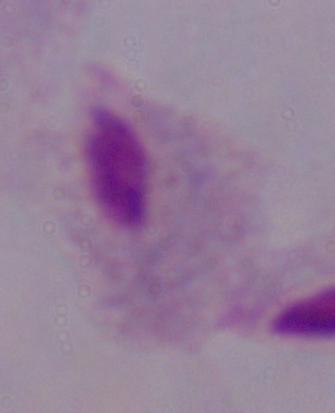
Photomicrograph. A trichomonad is seen. Captured at 1000x magnification.